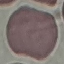
result = no malaria parasites seen
capture = smartphone through the microscope eyepiece
preparation = thin blood smear
stain = Giemsa
image type = automatically extracted cell patch, resized to 64 × 64 pixels